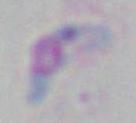
identification: Toxoplasma gondii
modality: photomicrograph
magnification: 1000x